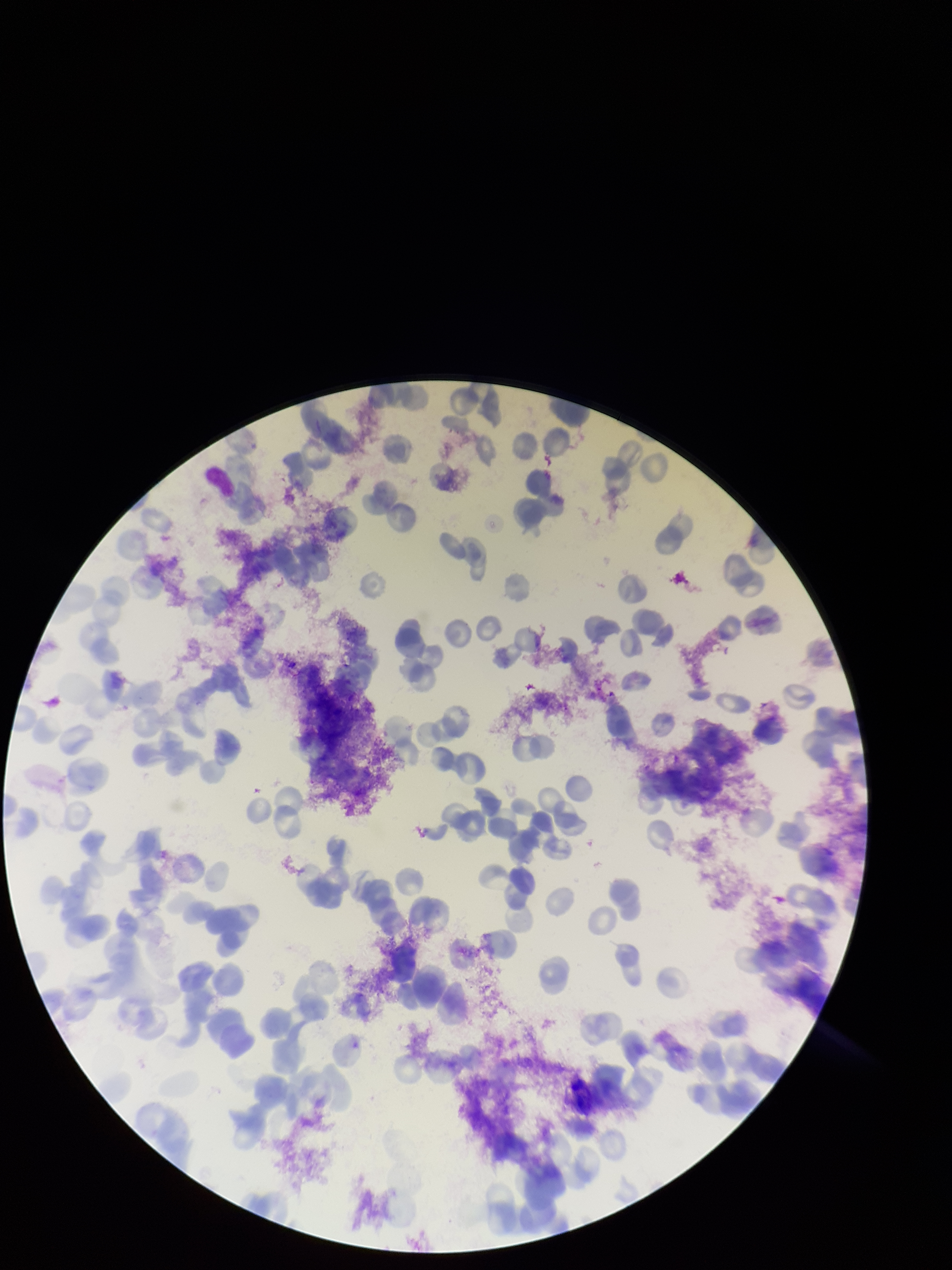

parasitized_red_blood_cells: none identified
capture: smartphone photograph through the microscope eyepiece
species_reported_for_this_patient: Plasmodium vivax
patient_malaria_status: infected
parasitized_red_blood_cell_count: 0
field_of_view: one from this slide
preparation: thin smear
red_blood_cell_count: 144
image_size: 952×1270 pixels
stain: Giemsa